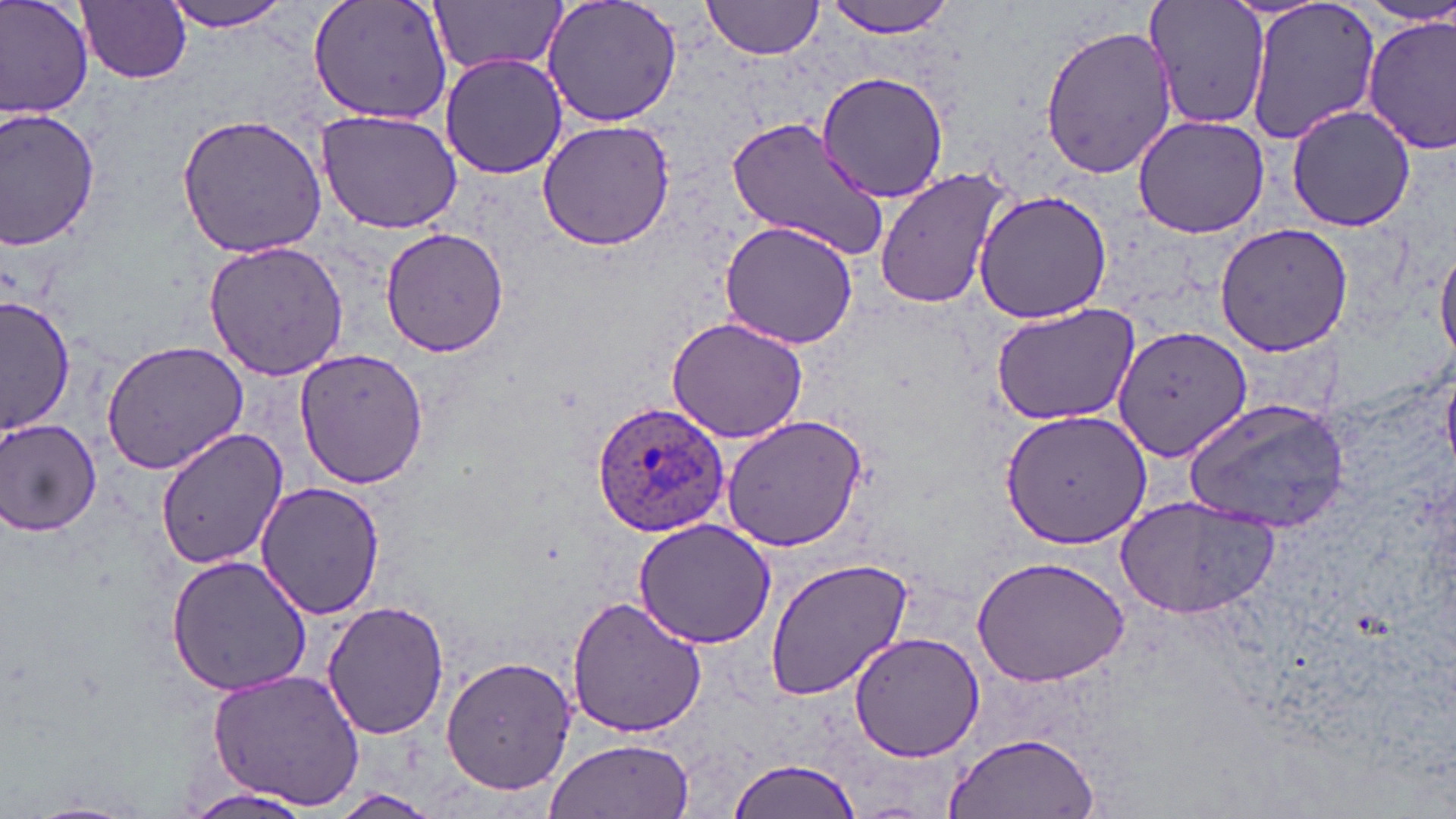
slide_level_diagnosis: Plasmodium ovale
field_of_view: one of a larger specimen
stain: May-Grünwald-Giemsa
plasmodium_ovale_infected_red_blood_cell_locations: 'approximate bounding boxes as [x1, y1, x2, y2] in pixels: [590, 400, 734, 538]'
image_size: 1456×819 pixels
preparation: thin blood film
uninfected_red_blood_cell_locations: 'approximate bounding boxes as [x1, y1, x2, y2] in pixels: [1, 0, 95, 121], [162, 0, 297, 33], [308, 0, 457, 127], [541, 0, 682, 128], [702, 0, 826, 60], [824, 0, 959, 38], [1143, 0, 1273, 135], [78, 1, 191, 85], [429, 1, 564, 77], [1244, 2, 1380, 148], [1362, 14, 1456, 158], [1039, 23, 1178, 182], [440, 53, 566, 179], [814, 72, 951, 204], [1286, 103, 1418, 232], [0, 108, 101, 250], [315, 109, 463, 235], [175, 112, 331, 260], [726, 114, 891, 261], [1132, 115, 1270, 239], [537, 119, 675, 251], [874, 165, 1014, 312], [974, 189, 1112, 325], [717, 221, 861, 351], [1212, 222, 1353, 358], [379, 226, 512, 359], [202, 241, 348, 379], [1436, 246, 1456, 367], [1, 293, 76, 439], [988, 299, 1139, 427], [666, 314, 808, 444], [1111, 325, 1252, 465], [99, 339, 250, 474], [294, 349, 428, 488], [1442, 369, 1456, 474], [1185, 397, 1352, 536], [1000, 408, 1152, 546], [719, 415, 867, 551], [1, 416, 103, 538], [154, 425, 289, 569], [255, 482, 385, 620], [1114, 494, 1282, 618], [632, 516, 775, 649], [165, 555, 312, 697], [971, 555, 1132, 688], [766, 559, 915, 700], [566, 594, 707, 738], [321, 601, 450, 741], [848, 631, 983, 762], [441, 655, 577, 795], [206, 669, 365, 809], [944, 731, 1100, 818], [542, 739, 696, 819], [726, 757, 862, 819], [180, 787, 318, 819], [329, 789, 444, 818]'
magnification: 1000x
modality: optical microscopy